Point out each leukocyte.
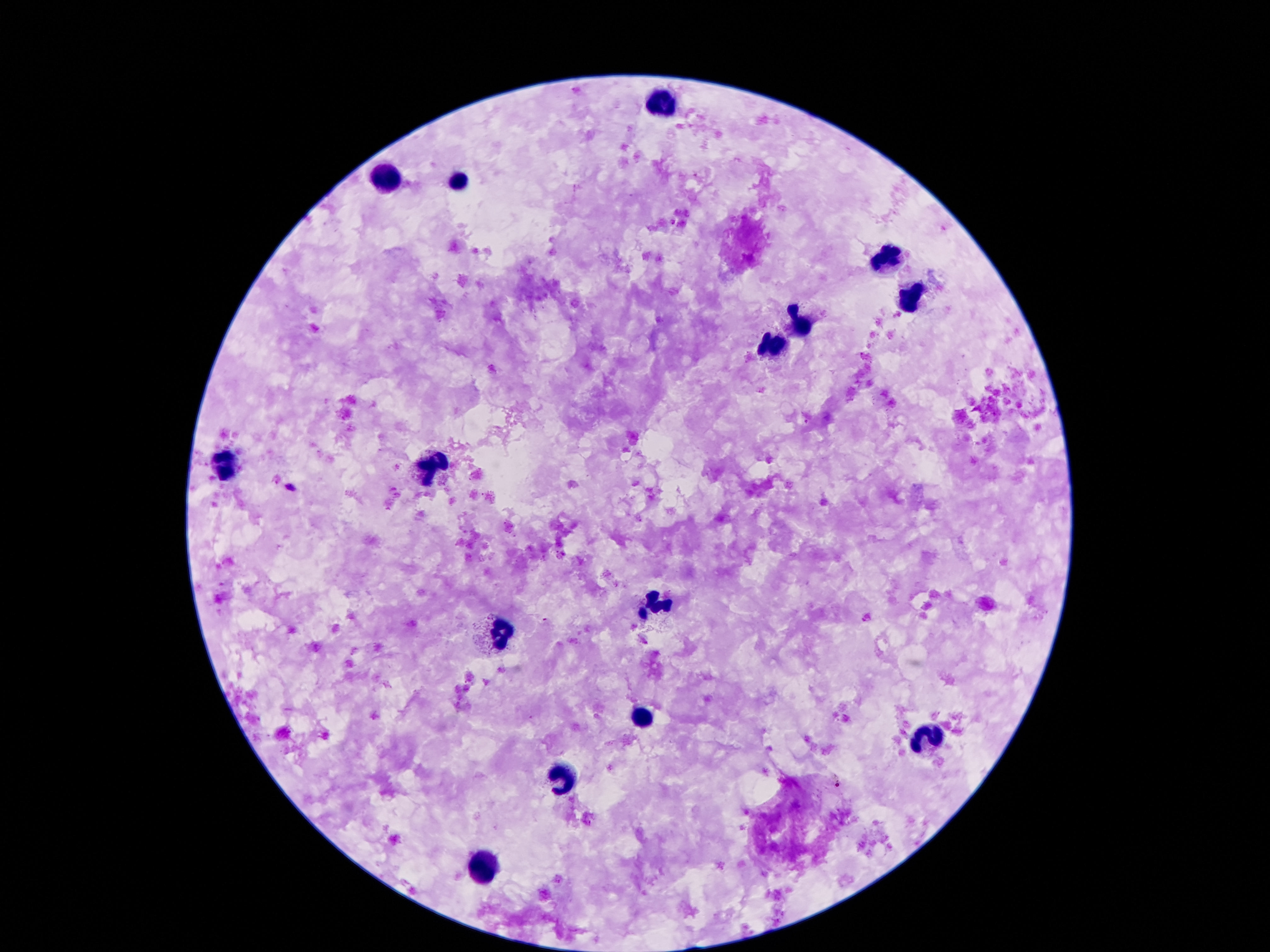
Approximate centers as {x, y} in pixels.
Leukocytes: {664, 105}, {382, 175}, {460, 183}, {886, 259}, {910, 299}, {802, 323}, {772, 349}, {226, 463}, {432, 469}, {658, 601}, {502, 633}, {642, 715}, {933, 741}, {564, 777}, {478, 865}.

Thick peripheral-blood smear. One field from this slide. Image is 1270×952 pixels. Photographed through the microscope eyepiece with a smartphone camera. 100x magnification. Giemsa stain. Patient malaria status: uninfected.